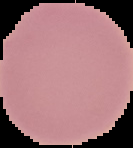
Summary:
  - Image type: segmented cell region with the area outside set to black
  - Preparation: thin blood smear
  - Image size: 133×148 pixels
  - Result: negative for Plasmodium parasites